State which parasite is depicted.
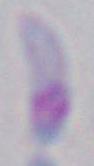

This is Toxoplasma gondii.

Micrograph. Captured at 1000x magnification.